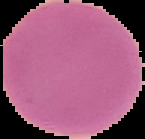

preparation = thin blood film
malaria status = uninfected
image type = segmented cell region on a black background
image size = 145×139 pixels